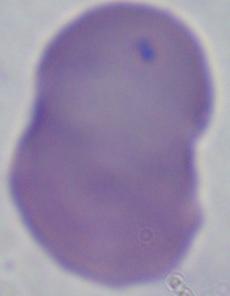

1000x magnification. Micrograph. A Babesia parasite is shown.